State the blood parasite species.
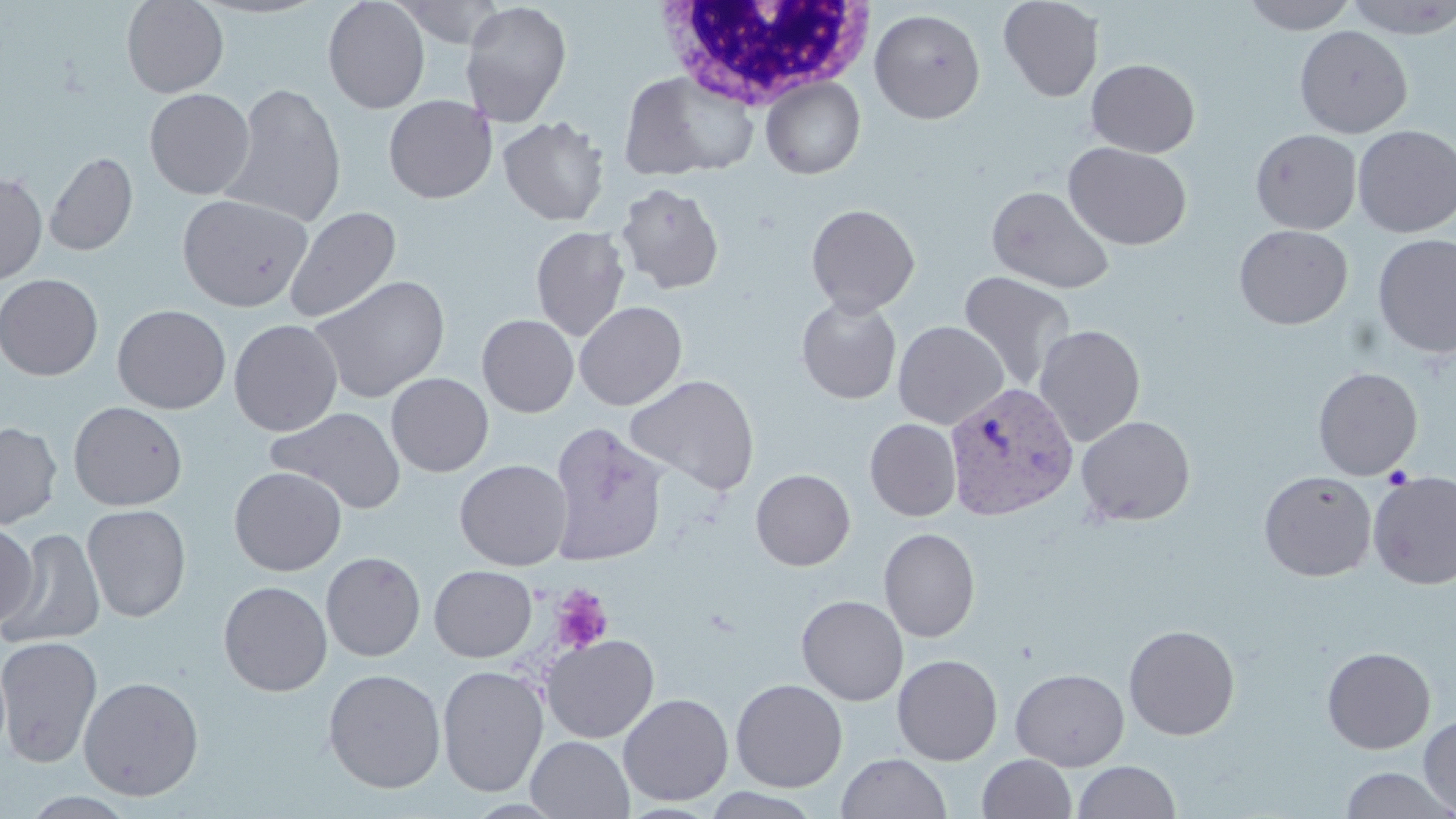

Plasmodium vivax.

Summary:
  - Coordinate format: approximate bounding boxes as named x1/y1/x2/y2 corners in pixels
  - Plasmodium vivax-infected red blood cell locations: (x1=944, y1=381, x2=1080, y2=522)
  - Uninfected red blood cell locations: (x1=122, y1=0, x2=228, y2=97), (x1=323, y1=0, x2=430, y2=114), (x1=392, y1=0, x2=507, y2=47), (x1=998, y1=0, x2=1104, y2=102), (x1=1240, y1=0, x2=1360, y2=34), (x1=1343, y1=0, x2=1455, y2=39), (x1=459, y1=1, x2=573, y2=127), (x1=869, y1=8, x2=986, y2=124), (x1=1294, y1=25, x2=1412, y2=138), (x1=1085, y1=58, x2=1200, y2=158), (x1=618, y1=70, x2=760, y2=180), (x1=761, y1=77, x2=865, y2=179), (x1=220, y1=83, x2=346, y2=228), (x1=144, y1=88, x2=254, y2=199), (x1=383, y1=95, x2=498, y2=203), (x1=498, y1=115, x2=610, y2=226), (x1=510, y1=116, x2=621, y2=338), (x1=1353, y1=125, x2=1456, y2=237), (x1=1250, y1=129, x2=1362, y2=234), (x1=1064, y1=142, x2=1191, y2=250), (x1=44, y1=151, x2=138, y2=257), (x1=0, y1=172, x2=47, y2=285), (x1=615, y1=181, x2=725, y2=294), (x1=987, y1=185, x2=1115, y2=294), (x1=176, y1=193, x2=313, y2=311), (x1=806, y1=203, x2=920, y2=316), (x1=284, y1=206, x2=402, y2=324), (x1=1233, y1=224, x2=1353, y2=329), (x1=531, y1=225, x2=631, y2=342), (x1=1373, y1=233, x2=1456, y2=358), (x1=958, y1=271, x2=1077, y2=391), (x1=0, y1=273, x2=103, y2=381), (x1=308, y1=274, x2=451, y2=404), (x1=796, y1=297, x2=902, y2=404), (x1=574, y1=301, x2=687, y2=410), (x1=112, y1=304, x2=230, y2=414), (x1=477, y1=314, x2=579, y2=417), (x1=228, y1=318, x2=343, y2=436), (x1=893, y1=321, x2=1009, y2=430), (x1=1033, y1=324, x2=1146, y2=445), (x1=1313, y1=366, x2=1422, y2=480), (x1=386, y1=372, x2=494, y2=477), (x1=624, y1=374, x2=760, y2=495), (x1=68, y1=401, x2=188, y2=511), (x1=266, y1=406, x2=407, y2=515), (x1=1075, y1=415, x2=1196, y2=526), (x1=864, y1=418, x2=962, y2=521), (x1=0, y1=421, x2=62, y2=529), (x1=548, y1=421, x2=668, y2=567), (x1=454, y1=459, x2=573, y2=570), (x1=228, y1=466, x2=347, y2=576), (x1=751, y1=468, x2=855, y2=571), (x1=1258, y1=470, x2=1377, y2=582), (x1=1367, y1=471, x2=1456, y2=589), (x1=81, y1=504, x2=192, y2=623), (x1=1, y1=521, x2=39, y2=631), (x1=2, y1=527, x2=105, y2=648), (x1=878, y1=527, x2=980, y2=643), (x1=322, y1=551, x2=425, y2=662), (x1=429, y1=565, x2=537, y2=662), (x1=218, y1=581, x2=333, y2=696), (x1=796, y1=595, x2=908, y2=705), (x1=1123, y1=624, x2=1240, y2=740), (x1=540, y1=634, x2=659, y2=743), (x1=0, y1=636, x2=103, y2=768), (x1=1321, y1=646, x2=1435, y2=754), (x1=892, y1=654, x2=1003, y2=765), (x1=437, y1=665, x2=549, y2=797), (x1=322, y1=668, x2=446, y2=793), (x1=1011, y1=668, x2=1130, y2=770), (x1=78, y1=675, x2=204, y2=800), (x1=730, y1=678, x2=848, y2=792), (x1=618, y1=693, x2=734, y2=806), (x1=1418, y1=714, x2=1456, y2=817), (x1=526, y1=735, x2=634, y2=818), (x1=836, y1=752, x2=951, y2=819), (x1=977, y1=753, x2=1077, y2=818), (x1=1072, y1=760, x2=1181, y2=819), (x1=1339, y1=766, x2=1455, y2=819), (x1=18, y1=790, x2=140, y2=818)
  - White blood cell locations: (x1=651, y1=0, x2=874, y2=112)
  - Platelet locations: (x1=551, y1=585, x2=613, y2=654)
  - Image size: 1456×819 pixels
  - Preparation: thin blood smear
  - Field of view: single
  - Stain: May-Grünwald-Giemsa
  - Modality: light microscopy
  - Magnification: 1000x